Locate every uninfected red blood cell.
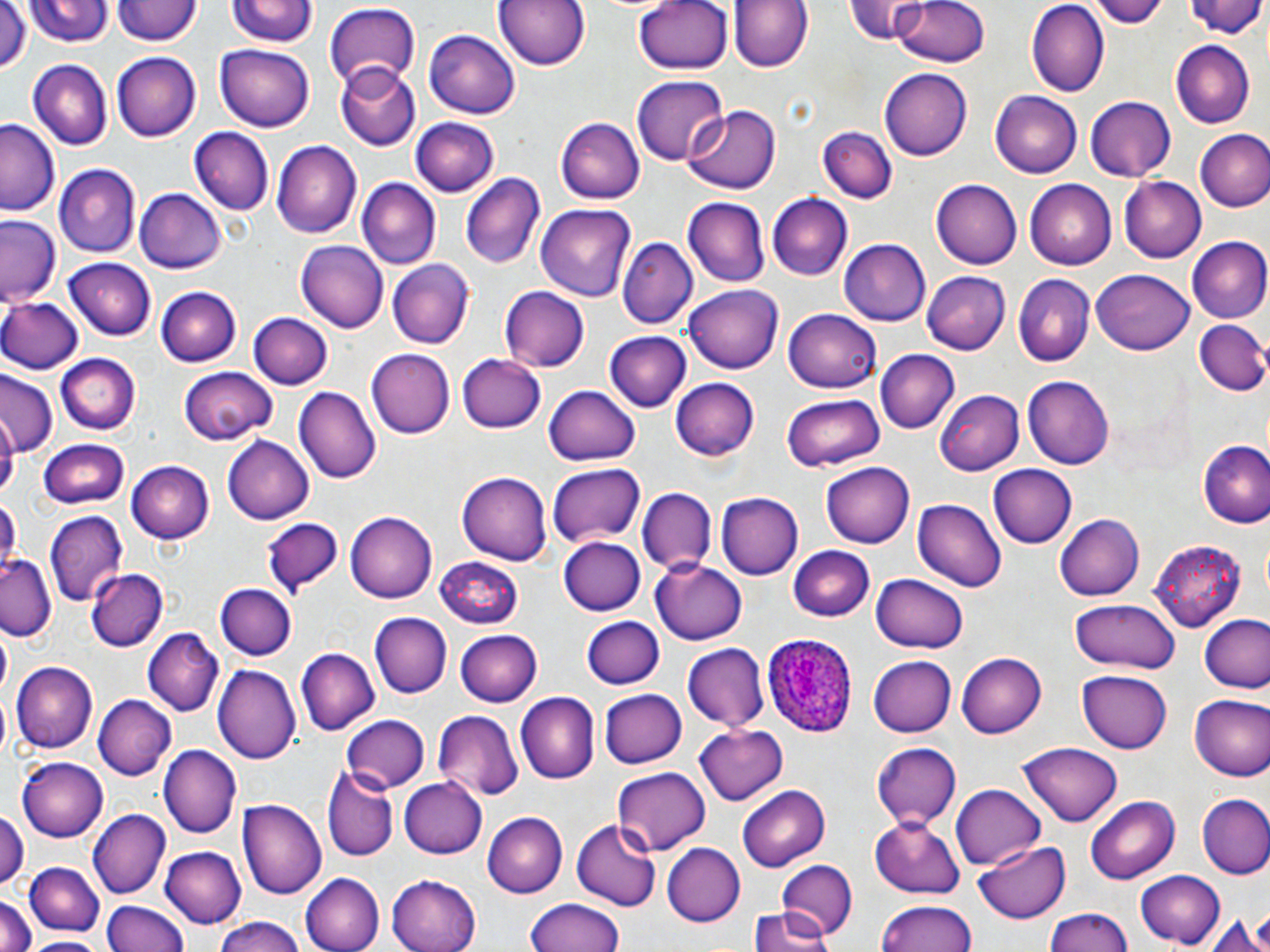
Approximate bounding boxes as (x1, y1, x2, y2) in pixels.
Uninfected red blood cells: (23, 0, 113, 47), (492, 0, 592, 72), (634, 0, 734, 75), (730, 0, 811, 73), (848, 0, 927, 44), (888, 0, 995, 66), (1026, 0, 1111, 96), (1091, 0, 1172, 28), (1189, 0, 1269, 45), (112, 1, 199, 47), (229, 1, 316, 51), (0, 3, 29, 75), (323, 4, 421, 86), (423, 29, 520, 118), (1171, 41, 1255, 128), (216, 43, 314, 133), (113, 50, 202, 143), (27, 58, 113, 152), (334, 61, 421, 151), (879, 68, 973, 161), (630, 76, 728, 166), (991, 92, 1082, 177), (1087, 96, 1176, 181), (683, 105, 782, 194), (554, 115, 645, 206), (411, 116, 499, 197), (0, 118, 62, 216), (188, 127, 274, 216), (819, 128, 895, 204), (1195, 129, 1270, 213), (270, 140, 362, 239), (55, 164, 140, 258), (459, 173, 545, 271), (1120, 176, 1206, 263), (357, 179, 441, 270), (1025, 179, 1117, 268), (931, 180, 1022, 268), (135, 188, 228, 274), (766, 194, 852, 279), (683, 199, 769, 286), (536, 204, 635, 300), (1, 214, 63, 309), (618, 235, 698, 327), (1186, 236, 1270, 323), (837, 239, 931, 325), (295, 241, 388, 332), (63, 257, 156, 340), (387, 260, 474, 349), (1091, 268, 1196, 356), (922, 270, 1009, 354), (1013, 274, 1095, 366), (686, 285, 783, 374), (155, 287, 241, 366), (500, 287, 591, 372), (0, 298, 81, 374), (784, 310, 881, 394), (250, 313, 332, 388), (1193, 318, 1268, 398), (606, 330, 691, 412), (366, 349, 456, 438), (876, 349, 958, 432), (57, 352, 140, 433), (456, 353, 547, 435), (178, 365, 276, 445), (1, 372, 60, 457), (1023, 377, 1114, 469), (672, 378, 758, 461), (294, 385, 381, 483), (545, 385, 641, 466), (935, 390, 1025, 474), (781, 393, 885, 473), (223, 436, 315, 524), (38, 439, 131, 510), (1201, 442, 1270, 529), (126, 459, 215, 543), (822, 461, 915, 547), (547, 464, 646, 548), (988, 466, 1077, 550), (456, 471, 551, 564), (637, 487, 715, 578), (715, 492, 804, 580), (0, 497, 19, 571), (914, 499, 1006, 593), (345, 509, 436, 602), (45, 510, 128, 606), (1056, 514, 1143, 601), (261, 518, 341, 601), (559, 537, 644, 616), (1147, 538, 1246, 628), (787, 546, 875, 621), (0, 552, 57, 640), (435, 556, 525, 627), (650, 563, 750, 645), (85, 568, 166, 650), (870, 574, 967, 654), (216, 583, 296, 661), (1070, 599, 1181, 674), (370, 612, 451, 698), (1198, 612, 1270, 697), (582, 617, 665, 690), (144, 629, 223, 716), (455, 629, 542, 707), (681, 643, 770, 732), (297, 646, 380, 734), (957, 651, 1047, 737), (867, 653, 956, 736), (11, 661, 97, 753), (215, 664, 300, 763), (1078, 670, 1172, 753), (597, 687, 687, 770), (518, 692, 600, 784), (94, 694, 176, 778), (1188, 695, 1269, 779), (433, 709, 524, 802), (341, 715, 430, 793), (695, 723, 788, 805), (872, 740, 960, 827), (1021, 740, 1122, 824), (158, 744, 240, 838), (17, 756, 107, 843), (322, 763, 396, 860), (610, 767, 710, 855), (398, 777, 486, 858), (952, 783, 1049, 870), (738, 785, 830, 871), (1086, 794, 1180, 881), (1198, 794, 1270, 879), (237, 798, 326, 900), (89, 808, 169, 899), (0, 810, 24, 893), (483, 812, 567, 897), (868, 815, 966, 898), (573, 820, 661, 911), (975, 839, 1070, 922), (662, 843, 744, 926), (160, 846, 247, 928), (774, 857, 860, 938), (26, 860, 103, 936), (1134, 870, 1226, 949), (301, 872, 383, 952), (387, 873, 480, 952), (0, 895, 35, 952), (526, 898, 627, 952), (876, 898, 980, 952), (104, 901, 187, 952), (1244, 903, 1270, 951), (1039, 906, 1137, 952), (1207, 909, 1266, 951), (750, 910, 834, 952), (210, 916, 308, 952), (22, 935, 112, 951).

slide-level diagnosis = Plasmodium ovale
preparation = thin blood film
field of view = single
image size = 1270×952 pixels
stain = May-Grünwald-Giemsa
magnification = 1000x
modality = light microscopy
Plasmodium ovale-infected red blood cell locations = approximate bounding boxes as (x1, y1, x2, y2) in pixels: (763, 635, 858, 738)